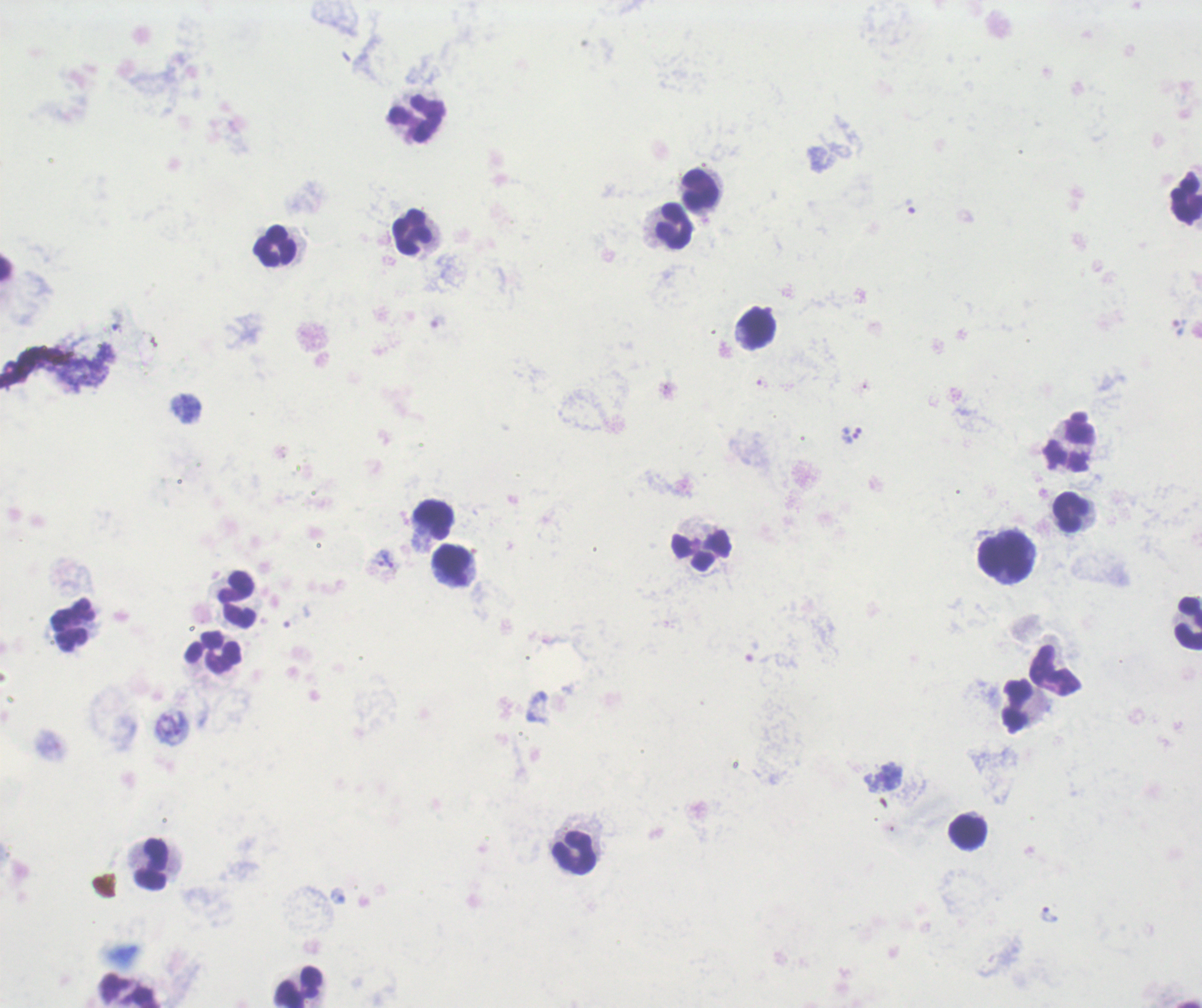
Approximate object centers, in pixels from the top-left corner. Trophozoite locations: (x=910, y=207), (x=1178, y=327), (x=851, y=439), (x=388, y=558), (x=1047, y=913). Leukocyte locations: (x=417, y=119), (x=699, y=189), (x=1186, y=197), (x=673, y=226), (x=412, y=231), (x=274, y=245), (x=755, y=328), (x=1070, y=441), (x=1072, y=512), (x=433, y=521), (x=701, y=550), (x=1005, y=559), (x=454, y=565), (x=237, y=599), (x=1187, y=623), (x=72, y=625), (x=214, y=652), (x=1056, y=671), (x=1017, y=705), (x=968, y=832), (x=575, y=852), (x=152, y=862), (x=299, y=986). Single field of view. 100x magnification. Romanowsky-stained preparation. Thick smear of blood. Image is 1202×1008 pixels. Result: Plasmodium parasites detected. Previously used in an actual diagnosis. Background quality: poor.